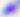

Summary:
  - Identification: Toxoplasma gondii
  - Magnification: 400x
  - Modality: micrograph